Describe the morphology of the erythrocytes.
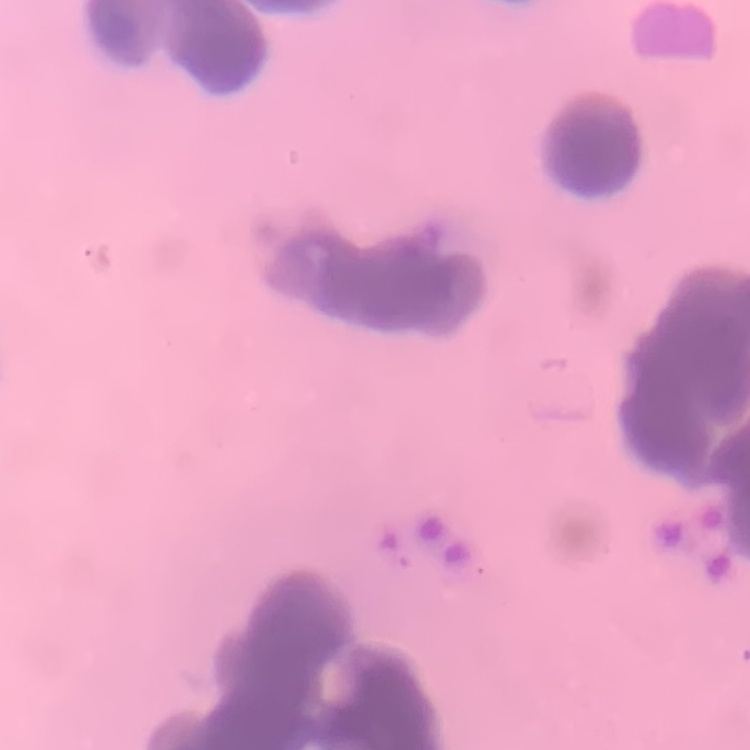

Rouleaux formation.

{
  "stain": "Field's or Giemsa",
  "preparation": "thin blood smear",
  "image_type": "square crop of a larger photomicrograph"
}